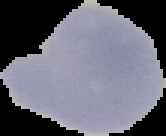 Segmented cell region on a black background. Result: malaria parasites identified. Image is 166×136 pixels. From a thin blood film.